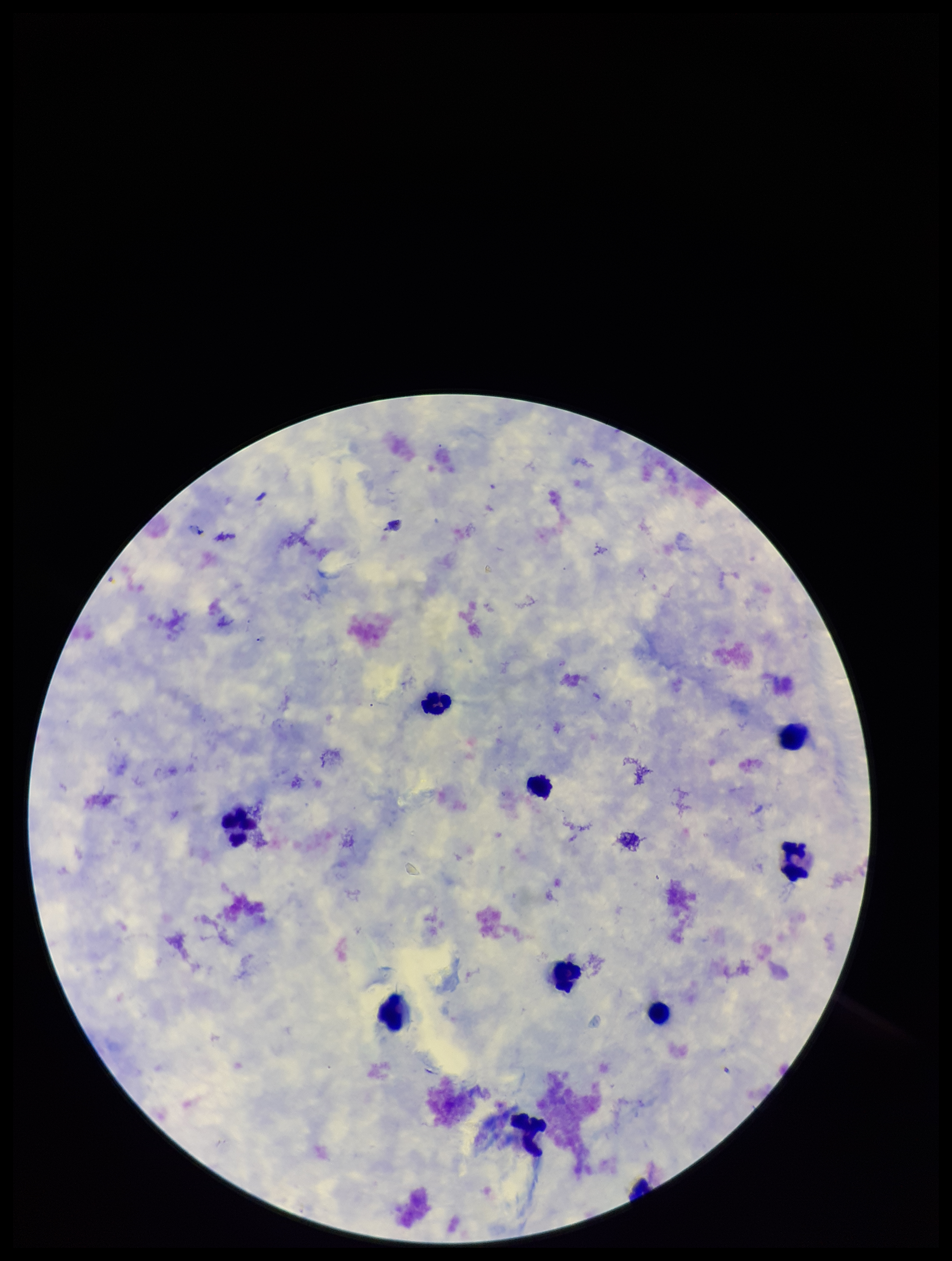
Summary:
  - Stain: Giemsa
  - Leukocyte count: 9
  - Patient malaria status: negative
  - Parasite count: 0
  - Field of view: single
  - Preparation: thick blood smear
  - Plasmodium parasites: none seen
  - Image size: 952×1261 pixels
  - Capture: smartphone photograph through the microscope eyepiece